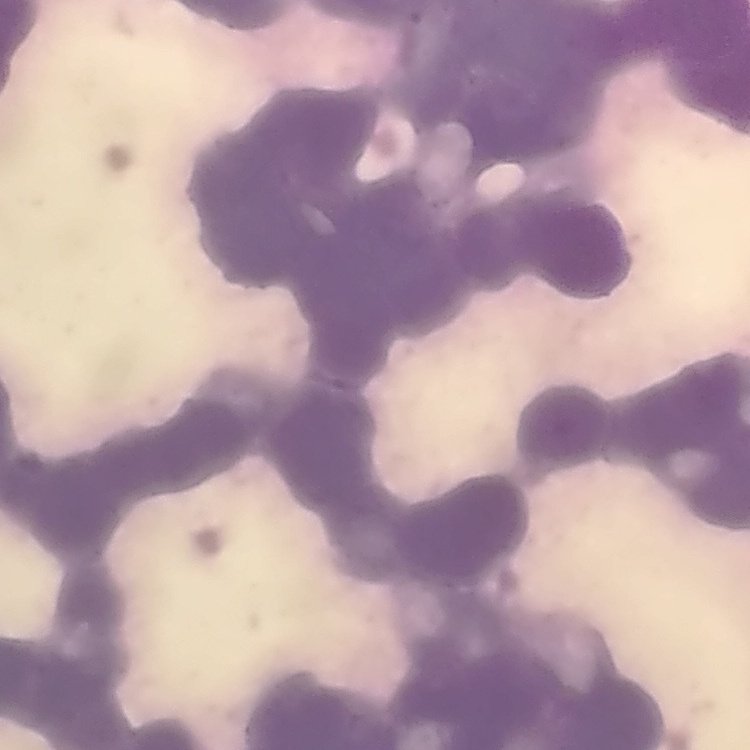 The erythrocytes show rouleaux formation. One tile cut from a larger photomicrograph. Thin blood film. Field's or Giemsa stain.